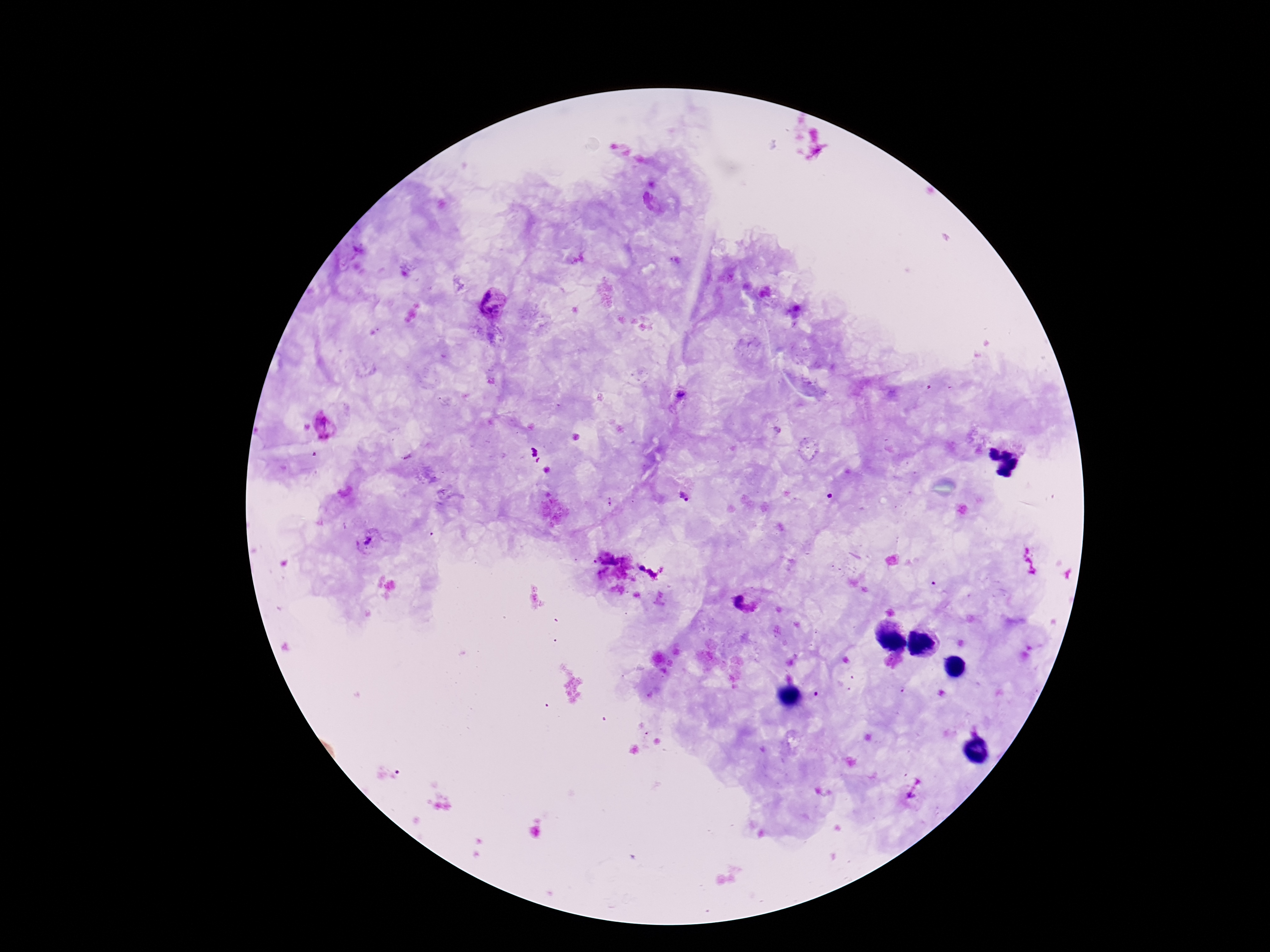

{
  "stain": "Giemsa",
  "capture": "smartphone camera through the microscope eyepiece",
  "plasmodium_parasite_locations": "approximate centers as (x, y) in pixels: (655, 205), (493, 301), (681, 397), (325, 425), (684, 497), (609, 502), (369, 541), (744, 603), (911, 796)",
  "preparation": "thick blood film",
  "magnification": "100x",
  "patient_malaria_status": "infected",
  "image_size": "1270×952 pixels",
  "field_of_view": "single"
}